Name the parasite shown.
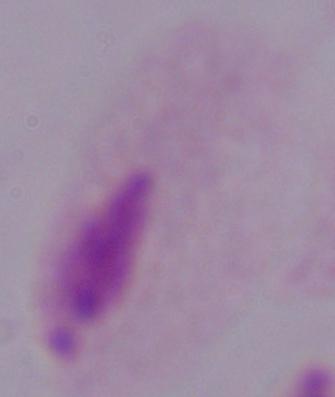
This is a trichomonad.

Captured at 1000x magnification. Photomicrograph.